Locate and identify every blood parasite.
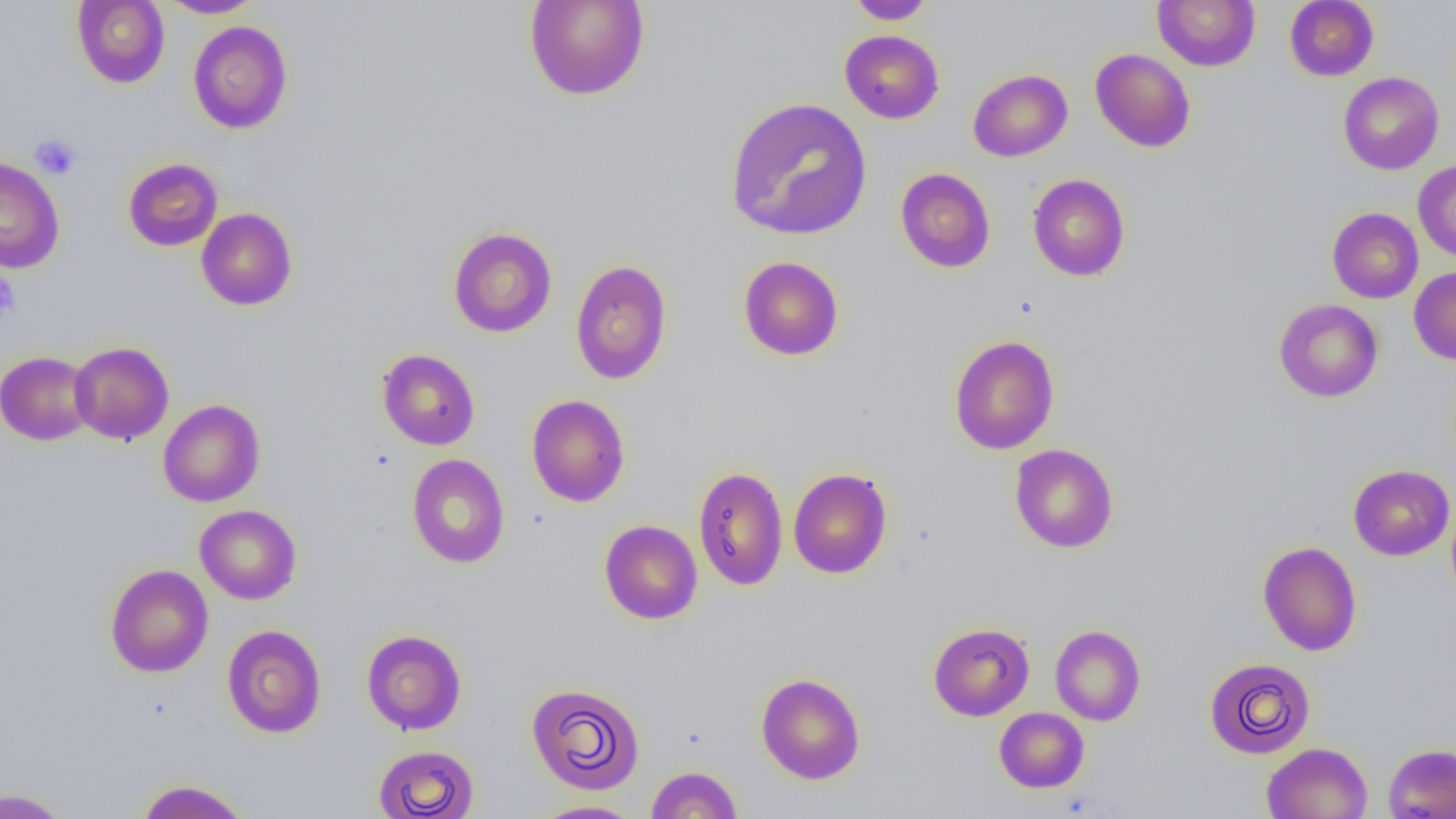

No blood parasites seen.

slide-level diagnosis = negative for blood parasites
field of view = single
magnification = 1000x
uninfected red blood cell locations = approximate bounding boxes as (x1,y1)-(x2,y2) corner pairs in pixels: (71,0)-(170,88), (158,0)-(264,18), (523,0)-(651,101), (846,0)-(936,24), (1152,0)-(1261,72), (1284,0)-(1379,81), (188,20)-(292,134), (840,29)-(944,123), (1090,48)-(1195,152), (967,69)-(1072,162), (1338,71)-(1444,174), (724,96)-(872,241), (0,157)-(64,274), (123,158)-(223,251), (1412,160)-(1456,261), (895,167)-(995,273), (1027,174)-(1130,281), (1327,207)-(1424,303), (196,208)-(297,310), (448,227)-(557,338), (738,256)-(844,361), (570,259)-(672,384), (1409,266)-(1456,365), (1273,299)-(1383,402), (948,335)-(1059,455), (69,341)-(174,444), (377,348)-(480,450), (0,351)-(96,445), (526,394)-(630,507), (158,399)-(265,507), (1009,443)-(1119,553), (407,453)-(510,569), (1348,464)-(1455,560), (693,466)-(789,591), (788,467)-(892,579), (195,505)-(301,605), (599,519)-(702,624), (1258,541)-(1362,656), (105,563)-(213,677), (928,622)-(1035,721), (1050,624)-(1146,726), (222,625)-(326,737), (361,629)-(467,735), (1204,657)-(1316,759), (756,673)-(866,784), (525,682)-(645,795), (994,707)-(1089,793), (1261,742)-(1373,819), (1383,743)-(1456,819), (373,744)-(479,818), (645,765)-(743,818), (135,779)-(251,819), (0,787)-(72,818), (530,799)-(642,819)
modality = optical microscopy
image size = 1456×819 pixels
preparation = thin blood film
platelet locations = approximate bounding boxes as (x1,y1)-(x2,y2) corner pairs in pixels: (30,133)-(80,179), (0,271)-(21,322)